State which parasite is depicted.
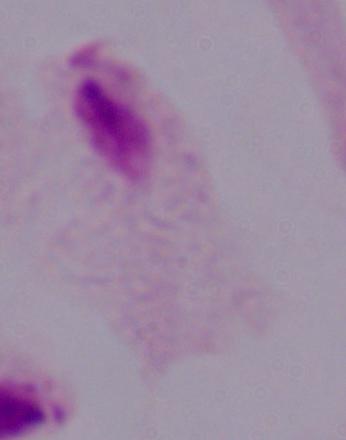
A trichomonad.

{
  "modality": "micrograph",
  "magnification": "1000x"
}